State which parasite is depicted.
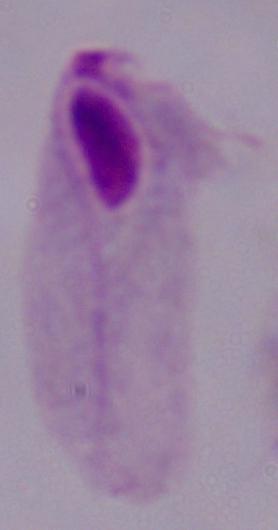

A trichomonad.

Photomicrograph. Captured at 1000x magnification.